State the blood parasite species.
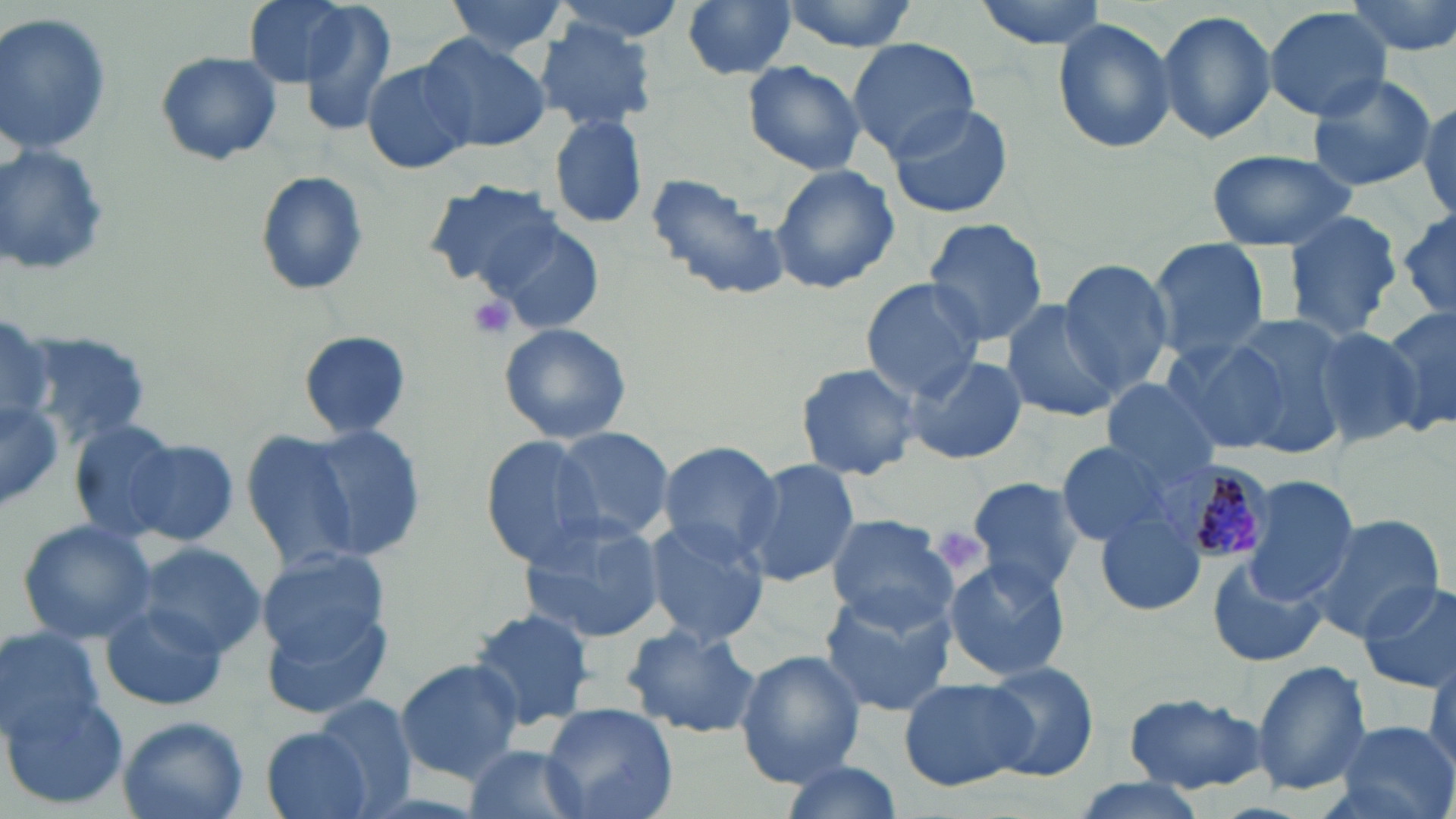
Plasmodium malariae.

Approximate bounding boxes as (x1,y1)-(x2,y2) corner pairs in pixels. Uninfected red blood cell locations: (241,0)-(360,89), (442,0)-(574,59), (549,0)-(688,44), (679,0)-(800,81), (973,0)-(1109,49), (1343,0)-(1456,59), (298,1)-(397,137), (776,1)-(921,50), (1265,6)-(1391,120), (1157,10)-(1277,144), (0,12)-(112,156), (1052,19)-(1178,154), (533,23)-(656,132), (416,33)-(552,152), (847,39)-(980,157), (155,50)-(283,167), (363,60)-(475,176), (741,62)-(866,175), (1306,72)-(1438,191), (1417,97)-(1455,222), (884,101)-(1015,221), (550,113)-(649,230), (0,144)-(114,282), (1205,148)-(1357,249), (766,164)-(901,294), (255,171)-(369,297), (644,171)-(790,302), (423,181)-(562,290), (1280,209)-(1403,343), (1397,211)-(1456,317), (487,218)-(602,335), (922,218)-(1051,347), (1148,239)-(1271,359), (1057,259)-(1175,398), (860,277)-(986,397), (1001,301)-(1122,423), (1378,305)-(1456,436), (0,314)-(52,435), (1223,317)-(1355,455), (1305,321)-(1429,450), (499,323)-(633,445), (20,329)-(154,447), (298,330)-(411,439), (1161,338)-(1290,454), (906,355)-(1026,466), (795,362)-(922,481), (1100,378)-(1223,487), (0,397)-(66,513), (65,418)-(189,543), (291,423)-(429,561), (548,426)-(675,542), (246,432)-(362,572), (481,436)-(606,568), (127,440)-(239,544), (1055,440)-(1178,547), (656,441)-(783,561), (738,459)-(863,589), (1241,475)-(1357,606), (967,476)-(1088,597), (1096,510)-(1206,618), (517,513)-(667,642), (1304,513)-(1443,645), (824,514)-(957,631), (16,518)-(156,646), (645,518)-(770,645), (134,543)-(266,659), (254,546)-(395,677), (942,557)-(1073,681), (1206,557)-(1324,668), (1358,580)-(1456,693), (818,594)-(955,717), (98,598)-(233,713), (258,599)-(392,718), (465,606)-(595,734), (623,623)-(763,739), (0,625)-(108,748), (735,648)-(866,785), (395,659)-(523,782), (1250,659)-(1372,797), (979,661)-(1099,781), (899,676)-(1031,790), (4,691)-(130,812), (1123,692)-(1268,793), (310,694)-(423,815), (541,701)-(680,819), (116,716)-(248,819), (1331,721)-(1455,819), (260,725)-(376,819), (462,744)-(588,819), (775,760)-(902,819), (1062,777)-(1213,819). Platelet locations: (465,292)-(518,341), (936,529)-(981,570). Plasmodium malariae-infected red blood cell locations: (1164,459)-(1273,565). Image is 1456×819 pixels. Single field of view. May-Grünwald-Giemsa-stained preparation. 1000x magnification. Light microscopy. Thin blood film.